Name the parasite shown.
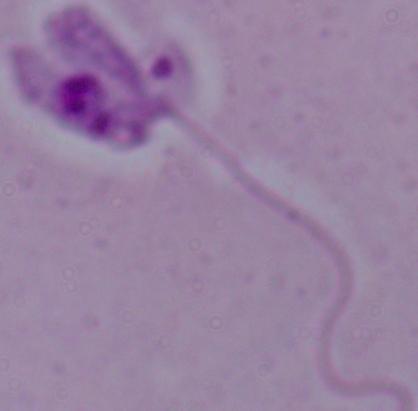
Leishmania.

Summary:
  - Magnification: 1000x
  - Modality: micrograph